Locate and identify every blood parasite.
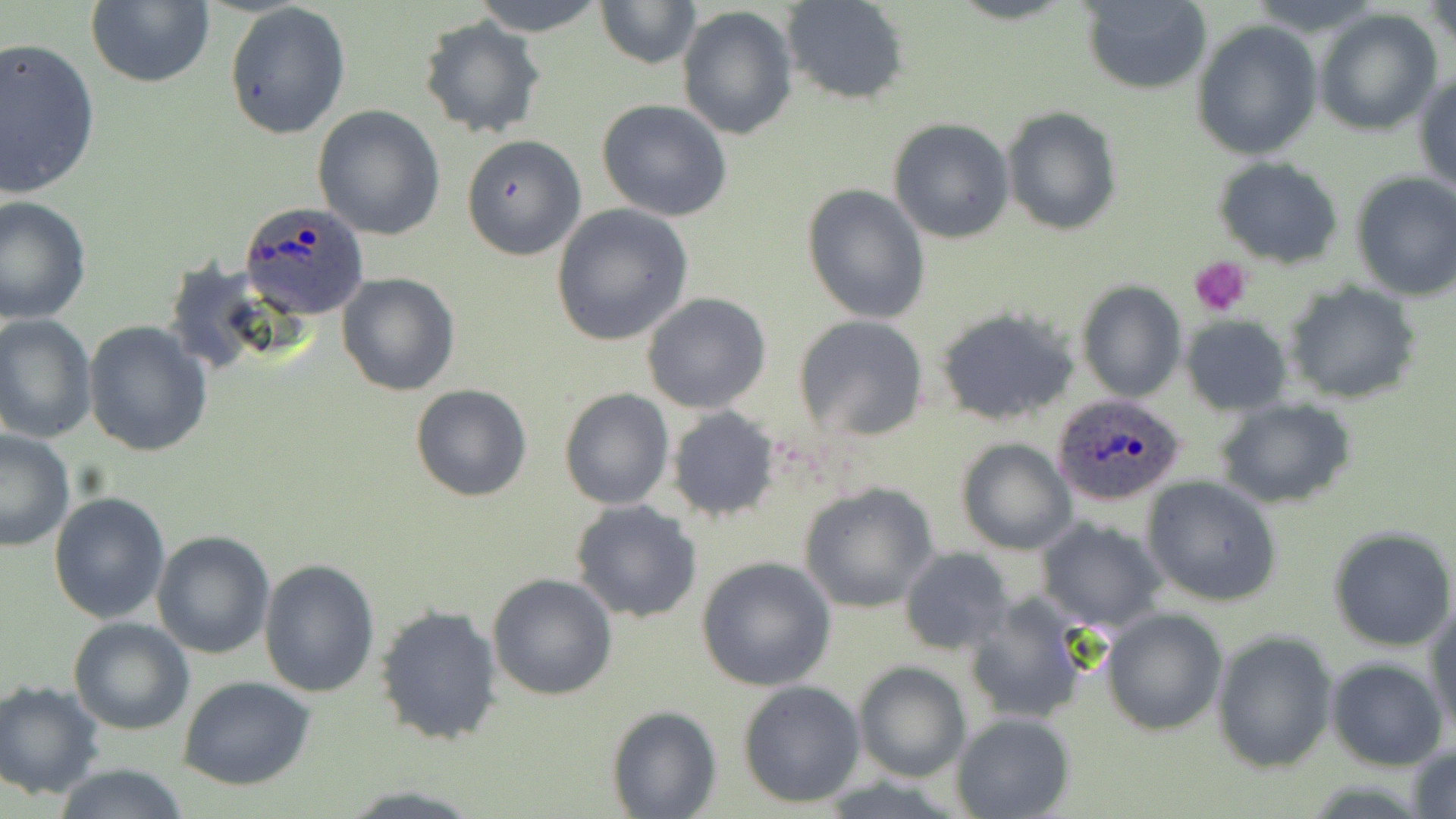
Approximate bounding boxes as (x1, y1, x2, y2) in pixels.
Plasmodium ovale-infected red blood cells: (238, 200, 371, 319), (1049, 392, 1187, 507).
No Plasmodium falciparum, Plasmodium malariae, Plasmodium vivax, Babesia divergens, or Trypanosoma brucei observed.

Summary:
  - Platelet locations: (1190, 256, 1250, 317)
  - Uninfected red blood cell locations: (85, 0, 216, 89), (468, 0, 607, 35), (595, 0, 700, 70), (782, 0, 911, 106), (1079, 1, 1212, 94), (223, 2, 351, 140), (1427, 2, 1454, 56), (677, 4, 798, 139), (1312, 8, 1442, 135), (417, 16, 547, 141), (1192, 20, 1321, 159), (0, 36, 101, 200), (1414, 68, 1456, 195), (596, 98, 733, 222), (312, 105, 445, 241), (1002, 107, 1122, 235), (888, 118, 1015, 244), (461, 135, 585, 260), (1213, 156, 1345, 268), (1349, 171, 1456, 302), (802, 183, 932, 324), (0, 194, 92, 324), (552, 203, 692, 345), (336, 271, 460, 396), (1077, 279, 1186, 401), (1285, 282, 1423, 404), (641, 292, 771, 413), (933, 306, 1081, 427), (0, 313, 97, 444), (793, 314, 930, 441), (1181, 316, 1292, 416), (82, 321, 213, 457), (409, 383, 532, 502), (558, 387, 674, 510), (1217, 399, 1356, 510), (666, 407, 781, 522), (0, 429, 77, 552), (954, 438, 1076, 555), (1142, 477, 1282, 607), (797, 482, 939, 614), (48, 491, 170, 625), (569, 500, 702, 623), (1035, 517, 1168, 633), (1329, 527, 1456, 650), (151, 531, 276, 659), (899, 546, 1016, 656), (694, 555, 838, 691), (259, 558, 381, 697), (487, 572, 620, 701), (962, 590, 1098, 726), (375, 603, 504, 747), (1427, 603, 1456, 736), (1100, 607, 1227, 734), (69, 617, 196, 735), (1212, 631, 1338, 773), (1325, 658, 1448, 771), (853, 661, 971, 782), (176, 675, 316, 790), (0, 679, 106, 799), (737, 680, 866, 808), (606, 704, 720, 818), (951, 712, 1076, 819), (1408, 741, 1456, 819), (51, 763, 192, 818)
  - Slide-level diagnosis: Plasmodium ovale
  - Preparation: thin blood film
  - Field of view: single
  - Modality: light microscopy
  - Magnification: 1000x
  - Image size: 1456×819 pixels
  - Stain: May-Grünwald-Giemsa